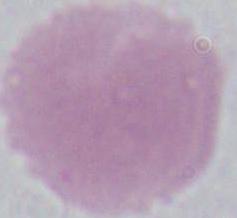 A red blood cell is shown. Photomicrograph. Captured at 1000x magnification.